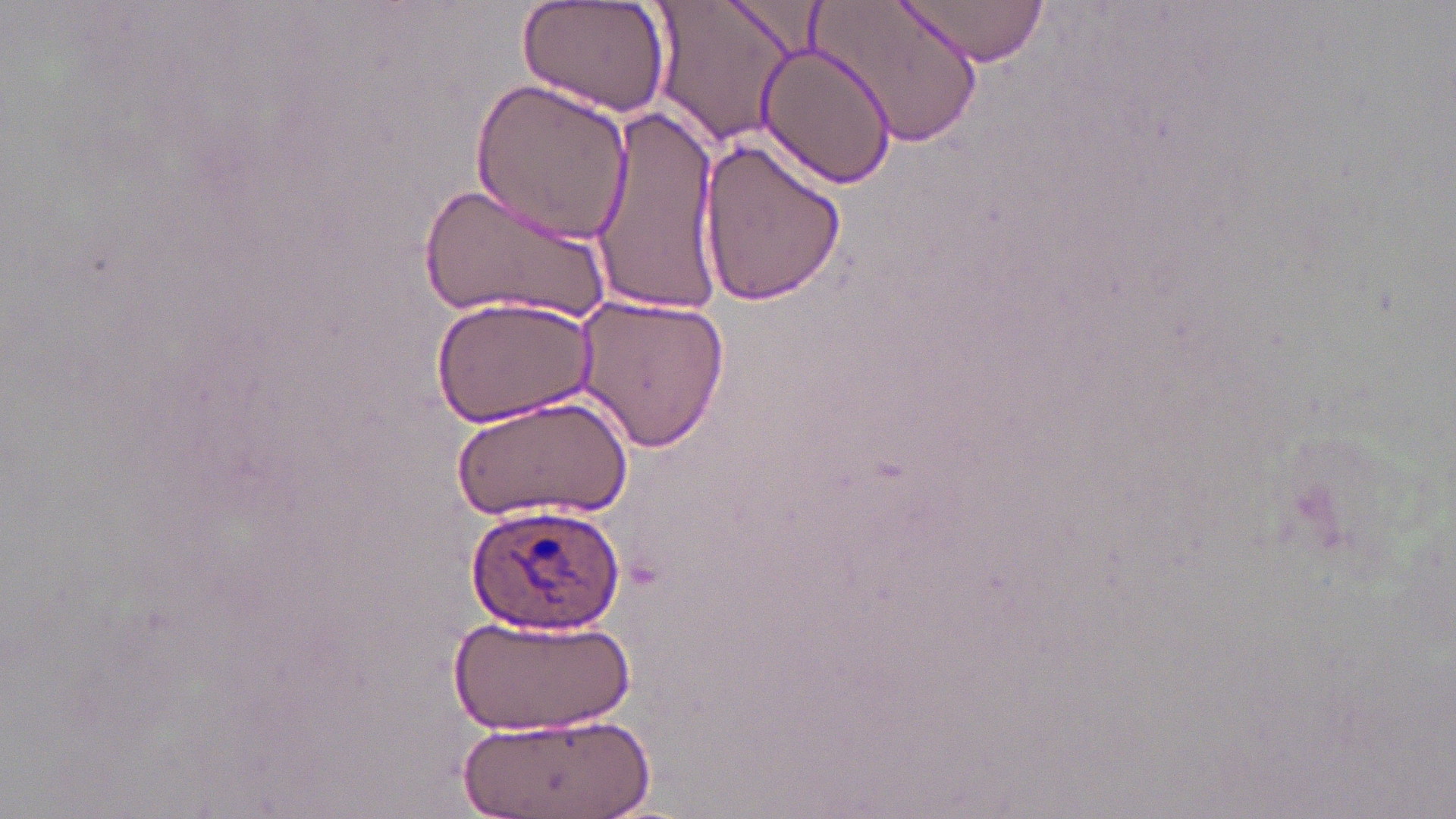
Summary:
  - Coordinate format: approximate bounding boxes as [x1, y1, x2, y2] in pixels
  - Plasmodium ovale-infected red blood cell locations: [466, 501, 627, 636]
  - Uninfected red blood cell locations: [513, 0, 670, 118], [648, 0, 803, 150], [813, 0, 982, 152], [893, 0, 1052, 68], [755, 38, 899, 190], [470, 75, 634, 245], [591, 107, 726, 315], [696, 133, 847, 306], [416, 177, 622, 328], [428, 293, 599, 431], [571, 293, 732, 454], [454, 392, 634, 521], [454, 613, 636, 733], [455, 715, 649, 818]
  - Slide-level diagnosis: Plasmodium ovale
  - Magnification: 1000x
  - Image size: 1456×819 pixels
  - Modality: light microscopy
  - Stain: May-Grünwald-Giemsa
  - Preparation: thin blood smear
  - Field of view: one of a larger specimen